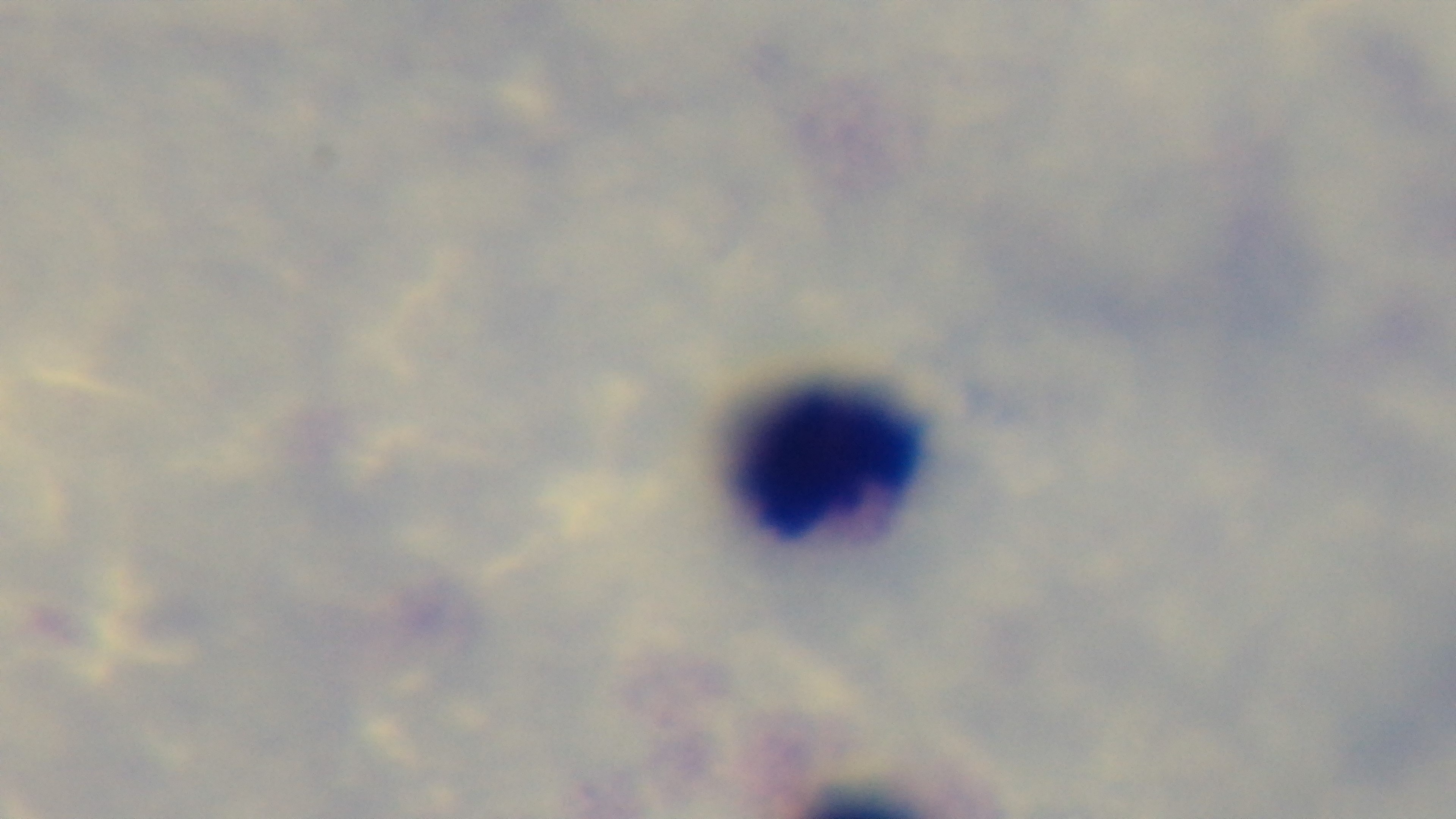

Mounted 4K digital camera. Preparation: thick smear. Giemsa-stained. One field from the slide. Malaria status: negative. Light microscopy. 100x oil-immersion objective.